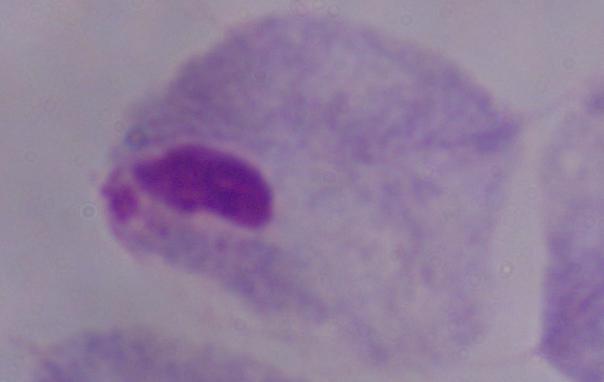

{
  "identification": "trichomonad",
  "magnification": "1000x",
  "modality": "photomicrograph"
}